Locate and identify every blood parasite.
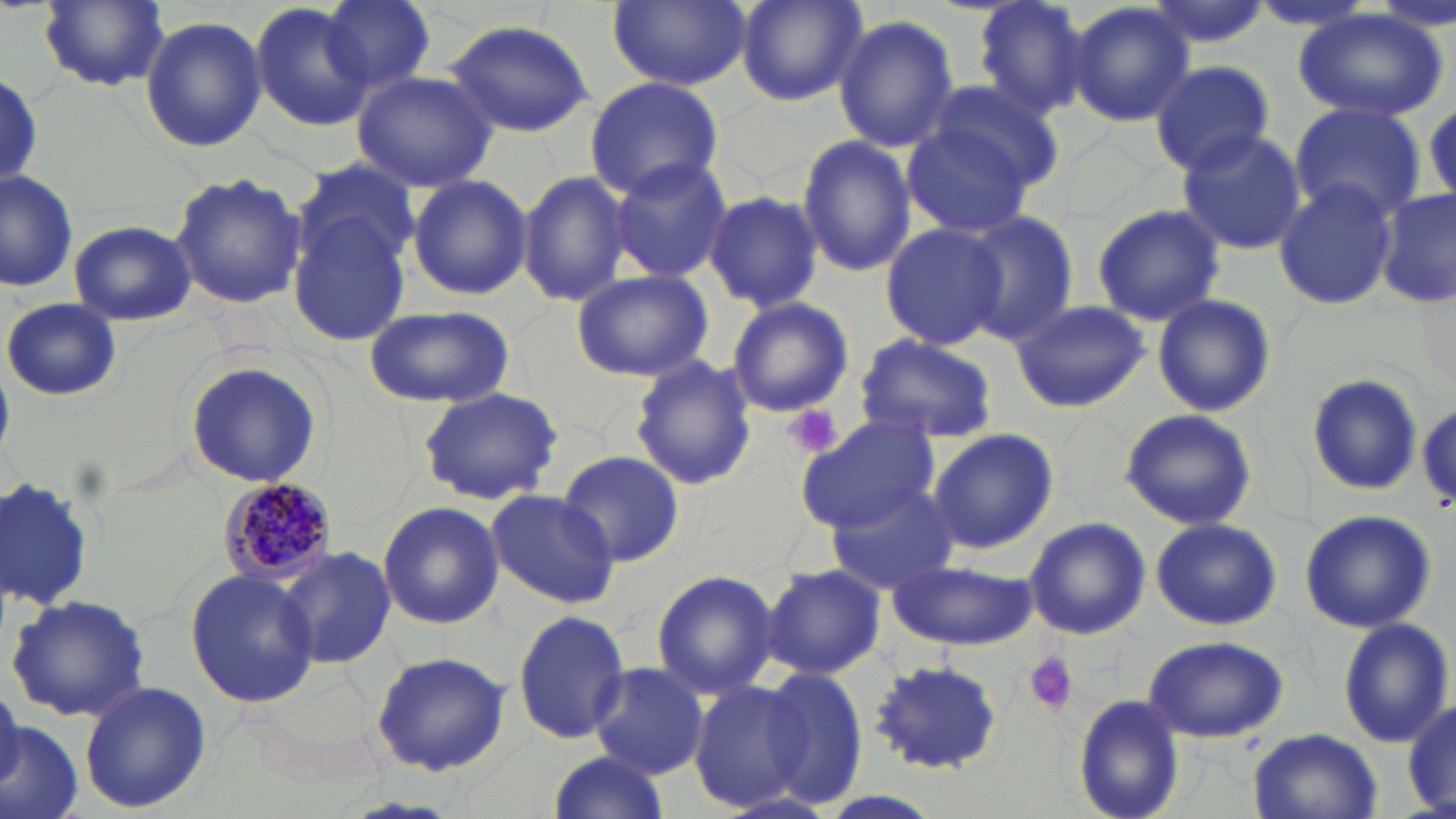

Approximate bounding boxes as [x1, y1, x2, y2] in pixels.
Plasmodium malariae-infected red blood cells: [217, 478, 336, 589].
No Plasmodium falciparum, Plasmodium ovale, Plasmodium vivax, Babesia divergens, or Trypanosoma brucei observed.

Platelet locations: [786, 406, 842, 457], [1025, 651, 1079, 715]. Uninfected red blood cell locations: [322, 0, 436, 92], [606, 0, 752, 90], [734, 0, 868, 107], [971, 0, 1091, 120], [38, 1, 170, 92], [1063, 1, 1196, 128], [1142, 1, 1274, 52], [251, 3, 374, 132], [1294, 11, 1448, 122], [834, 15, 959, 153], [141, 16, 265, 154], [443, 18, 596, 137], [1151, 60, 1275, 175], [350, 69, 498, 191], [0, 73, 44, 190], [585, 76, 724, 199], [918, 77, 1065, 194], [1288, 103, 1428, 222], [902, 121, 1039, 237], [1175, 130, 1308, 256], [796, 133, 916, 279], [609, 156, 735, 283], [293, 157, 423, 282], [518, 168, 632, 307], [0, 171, 80, 293], [170, 171, 307, 311], [406, 173, 532, 300], [1273, 178, 1398, 312], [1377, 187, 1454, 311], [701, 191, 824, 313], [1090, 203, 1224, 327], [289, 207, 415, 345], [958, 211, 1081, 343], [878, 220, 1010, 353], [69, 221, 196, 326], [570, 268, 716, 381], [1151, 293, 1277, 419], [725, 297, 853, 417], [3, 298, 121, 401], [1008, 299, 1150, 414], [363, 305, 516, 408], [854, 334, 997, 443], [629, 355, 758, 491], [185, 359, 323, 489], [0, 367, 15, 459], [1305, 373, 1423, 496], [416, 388, 562, 504], [1119, 409, 1260, 533], [795, 415, 942, 532], [926, 426, 1058, 555], [557, 449, 685, 569], [0, 477, 96, 610], [823, 484, 961, 592], [484, 487, 619, 608], [377, 501, 505, 629], [1298, 509, 1436, 633], [1024, 516, 1151, 641], [1150, 519, 1282, 631], [280, 545, 400, 670], [889, 558, 1035, 651], [763, 565, 885, 678], [186, 569, 318, 707], [650, 570, 778, 698], [6, 592, 152, 723], [513, 609, 631, 744], [1335, 617, 1453, 747], [1143, 635, 1289, 743], [371, 651, 512, 776], [868, 658, 1002, 773], [587, 663, 709, 779], [763, 667, 869, 808], [78, 680, 212, 813], [690, 682, 809, 811], [1074, 694, 1186, 819], [1401, 698, 1456, 814], [0, 719, 85, 819], [1247, 728, 1385, 819], [543, 752, 674, 818]. Slide-level diagnosis: Plasmodium malariae. May-Grünwald-Giemsa-stained preparation. Thin blood smear. One field of a larger specimen. Image is 1456×819 pixels. Light microscopy. Captured at 1000x magnification.